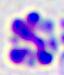
{
  "modality": "micrograph",
  "identification": "leukocyte",
  "magnification": "400x"
}